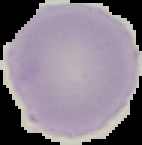 From a thin blood film. Image is 142×145 pixels. Segmented cell region on a black background. Malaria status: uninfected.